Assess this cell for malaria.
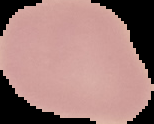

It is uninfected.

Image is 154×124 pixels. From a thin blood smear. The area outside the segmented cell region is set to black.